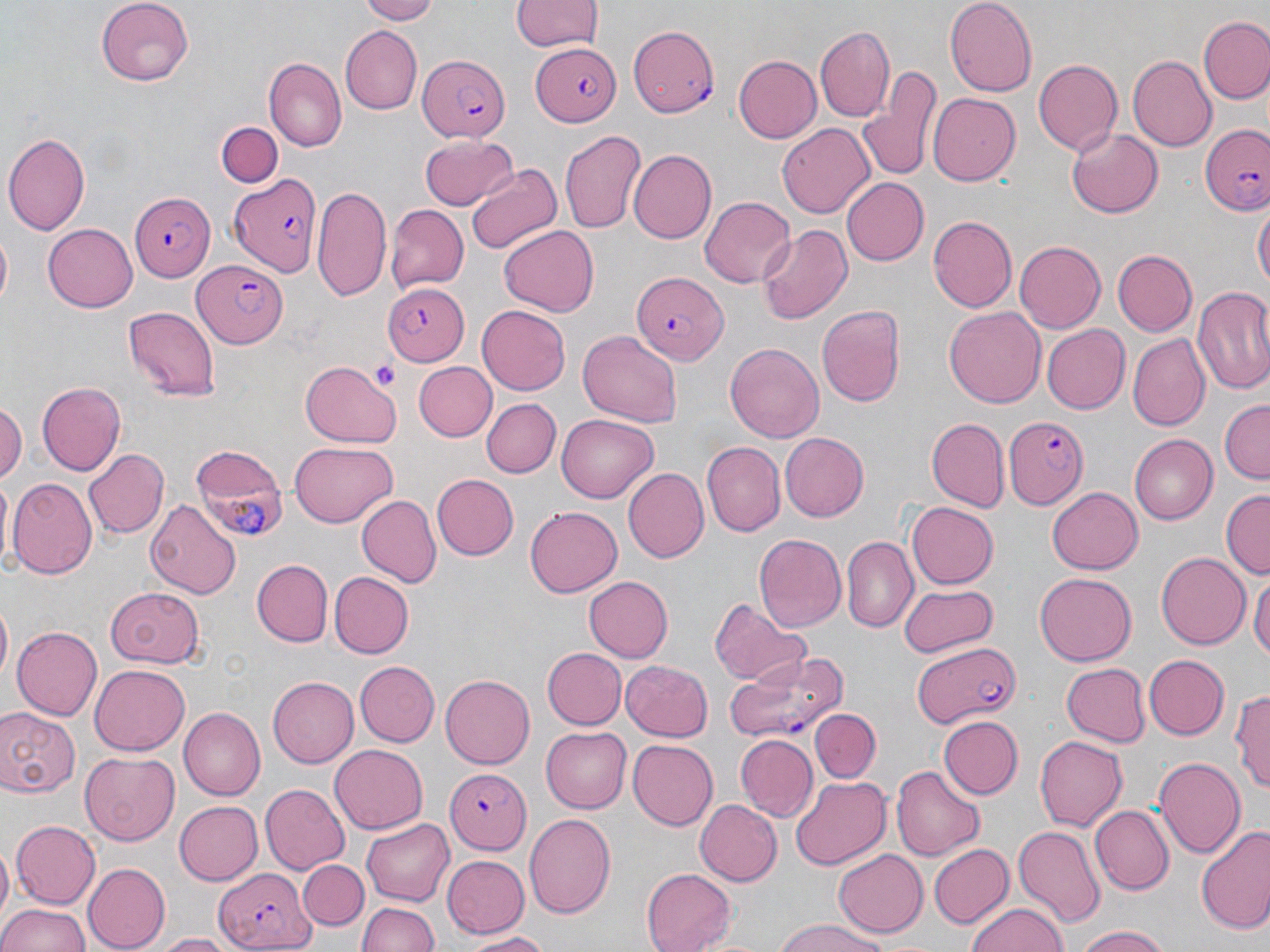
slide_level_diagnosis: Plasmodium falciparum
platelet_locations: 'approximate bounding boxes as named x1/y1/x2/y2 corners in pixels: (x1=372, y1=361, x2=397, y2=387)'
preparation: thin blood smear
field_of_view: single
image_size: 1270×952 pixels
magnification: 1000x
uninfected_red_blood_cell_locations: 'approximate bounding boxes as named x1/y1/x2/y2 corners in pixels: (x1=96, y1=0, x2=196, y2=85), (x1=358, y1=0, x2=438, y2=23), (x1=512, y1=0, x2=602, y2=54), (x1=945, y1=0, x2=1036, y2=93), (x1=1198, y1=14, x2=1270, y2=106), (x1=342, y1=26, x2=423, y2=114), (x1=815, y1=26, x2=896, y2=123), (x1=1128, y1=54, x2=1219, y2=150), (x1=733, y1=56, x2=821, y2=142), (x1=265, y1=58, x2=347, y2=152), (x1=1033, y1=59, x2=1123, y2=154), (x1=856, y1=65, x2=941, y2=184), (x1=928, y1=92, x2=1021, y2=186), (x1=215, y1=121, x2=284, y2=188), (x1=776, y1=123, x2=877, y2=219), (x1=559, y1=129, x2=646, y2=234), (x1=1067, y1=129, x2=1164, y2=217), (x1=4, y1=132, x2=90, y2=237), (x1=419, y1=137, x2=518, y2=210), (x1=629, y1=148, x2=717, y2=242), (x1=465, y1=163, x2=562, y2=257), (x1=840, y1=177, x2=928, y2=267), (x1=312, y1=186, x2=390, y2=301), (x1=700, y1=197, x2=797, y2=287), (x1=1254, y1=204, x2=1268, y2=294), (x1=386, y1=205, x2=467, y2=290), (x1=929, y1=215, x2=1017, y2=311), (x1=42, y1=224, x2=137, y2=313), (x1=498, y1=224, x2=597, y2=313), (x1=757, y1=225, x2=852, y2=325), (x1=1015, y1=241, x2=1105, y2=333), (x1=1113, y1=250, x2=1196, y2=336), (x1=1192, y1=289, x2=1270, y2=397), (x1=816, y1=304, x2=908, y2=408), (x1=123, y1=305, x2=221, y2=400), (x1=945, y1=305, x2=1046, y2=410), (x1=477, y1=306, x2=570, y2=395), (x1=1041, y1=324, x2=1129, y2=414), (x1=576, y1=330, x2=683, y2=426), (x1=1127, y1=333, x2=1209, y2=429), (x1=725, y1=341, x2=823, y2=445), (x1=299, y1=361, x2=399, y2=448), (x1=414, y1=362, x2=494, y2=441), (x1=36, y1=382, x2=125, y2=474), (x1=479, y1=398, x2=559, y2=478), (x1=0, y1=399, x2=26, y2=487), (x1=1218, y1=401, x2=1270, y2=482), (x1=557, y1=415, x2=658, y2=502), (x1=927, y1=419, x2=1007, y2=511), (x1=777, y1=433, x2=868, y2=523), (x1=1129, y1=434, x2=1218, y2=522), (x1=289, y1=442, x2=396, y2=526), (x1=702, y1=442, x2=783, y2=536), (x1=84, y1=447, x2=169, y2=537), (x1=623, y1=468, x2=711, y2=563), (x1=429, y1=473, x2=517, y2=561), (x1=6, y1=477, x2=98, y2=580), (x1=1048, y1=485, x2=1145, y2=575), (x1=1221, y1=492, x2=1269, y2=578), (x1=356, y1=494, x2=440, y2=587), (x1=146, y1=498, x2=240, y2=600), (x1=904, y1=500, x2=998, y2=589), (x1=525, y1=505, x2=622, y2=598), (x1=754, y1=532, x2=847, y2=635), (x1=842, y1=534, x2=918, y2=633), (x1=1154, y1=552, x2=1250, y2=651), (x1=251, y1=558, x2=332, y2=646), (x1=1035, y1=570, x2=1136, y2=663), (x1=328, y1=571, x2=414, y2=659), (x1=1251, y1=572, x2=1270, y2=665), (x1=582, y1=574, x2=671, y2=661), (x1=897, y1=583, x2=998, y2=657), (x1=103, y1=586, x2=204, y2=668), (x1=708, y1=595, x2=811, y2=687), (x1=1, y1=602, x2=13, y2=686), (x1=11, y1=625, x2=102, y2=722), (x1=541, y1=647, x2=625, y2=731), (x1=1142, y1=653, x2=1227, y2=740), (x1=356, y1=659, x2=440, y2=746), (x1=620, y1=661, x2=714, y2=741), (x1=1060, y1=663, x2=1150, y2=747), (x1=89, y1=666, x2=188, y2=755), (x1=440, y1=674, x2=534, y2=768), (x1=267, y1=676, x2=359, y2=768), (x1=1232, y1=684, x2=1270, y2=792), (x1=0, y1=707, x2=79, y2=797), (x1=179, y1=707, x2=267, y2=800), (x1=811, y1=707, x2=882, y2=782), (x1=939, y1=716, x2=1023, y2=801), (x1=542, y1=725, x2=631, y2=813), (x1=735, y1=734, x2=816, y2=821), (x1=1033, y1=735, x2=1127, y2=833), (x1=628, y1=740, x2=717, y2=831), (x1=329, y1=745, x2=428, y2=835), (x1=80, y1=751, x2=181, y2=845), (x1=1154, y1=756, x2=1245, y2=859), (x1=894, y1=763, x2=983, y2=860), (x1=790, y1=776, x2=891, y2=870), (x1=260, y1=785, x2=350, y2=874), (x1=693, y1=798, x2=781, y2=885), (x1=174, y1=801, x2=262, y2=885), (x1=1091, y1=804, x2=1174, y2=895), (x1=523, y1=810, x2=615, y2=918), (x1=361, y1=818, x2=454, y2=905), (x1=11, y1=820, x2=100, y2=909), (x1=1012, y1=824, x2=1106, y2=927), (x1=1196, y1=824, x2=1270, y2=935), (x1=930, y1=842, x2=1013, y2=929), (x1=834, y1=848, x2=927, y2=935), (x1=440, y1=855, x2=528, y2=937), (x1=299, y1=860, x2=367, y2=930), (x1=83, y1=863, x2=170, y2=950), (x1=642, y1=867, x2=738, y2=952), (x1=357, y1=900, x2=440, y2=952), (x1=0, y1=902, x2=92, y2=952), (x1=964, y1=902, x2=1071, y2=952), (x1=772, y1=919, x2=890, y2=952), (x1=1072, y1=925, x2=1172, y2=952), (x1=155, y1=931, x2=245, y2=951), (x1=457, y1=932, x2=555, y2=949)'
stain: May-Grünwald-Giemsa
modality: optical microscopy
plasmodium_falciparum_infected_red_blood_cell_locations: 'approximate bounding boxes as named x1/y1/x2/y2 corners in pixels: (x1=628, y1=24, x2=720, y2=115), (x1=531, y1=42, x2=622, y2=125), (x1=418, y1=53, x2=510, y2=143), (x1=1201, y1=123, x2=1270, y2=215), (x1=229, y1=172, x2=323, y2=279), (x1=126, y1=192, x2=213, y2=280), (x1=192, y1=261, x2=289, y2=349), (x1=630, y1=271, x2=726, y2=361), (x1=384, y1=280, x2=472, y2=365), (x1=1003, y1=417, x2=1090, y2=511), (x1=190, y1=446, x2=288, y2=542), (x1=911, y1=641, x2=1019, y2=729), (x1=725, y1=651, x2=853, y2=744), (x1=442, y1=768, x2=530, y2=851), (x1=214, y1=867, x2=314, y2=951)'